Report the malaria status of this cell.
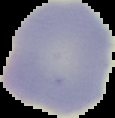
It is uninfected.

From a thin blood film. Image is 115×118 pixels. Segmented cell region on a black background.